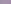
A trypanosome is seen. Photomicrograph. 1000x magnification.